Find the red blood cells and label each as P. falciparum-infected, uninfected, or of indeterminate infection status.
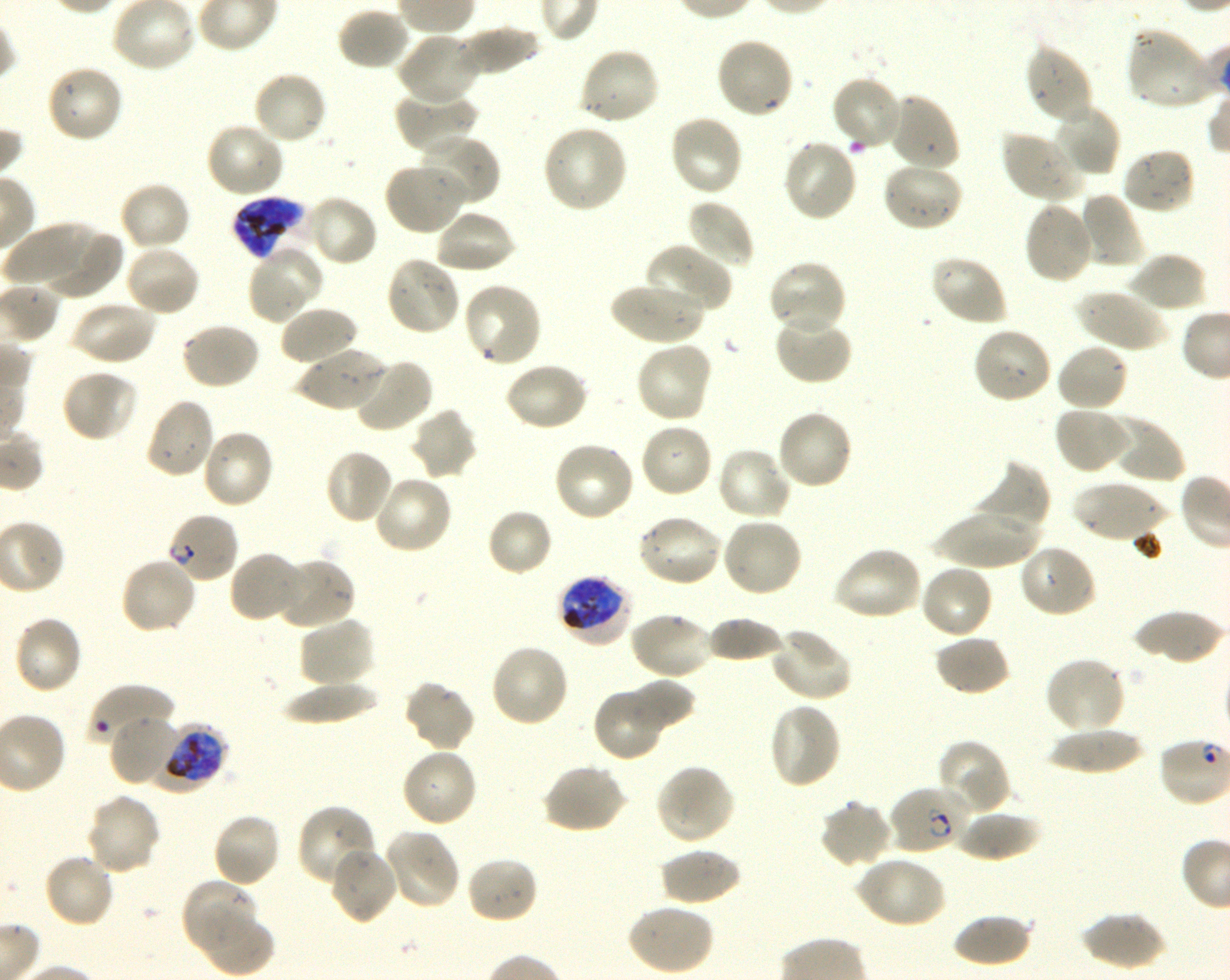
Approximate bounding boxes as {x1, y1, x2, y2} in pixels. Not every red blood cell is marked. A life-cycle stage — or a range of stages, where the recorded stages span more than one — follows each staged infected red blood cell.
Infected red blood cells: {232, 197, 309, 260} late trophozoite to late schizont; {167, 511, 239, 584} ring; {557, 573, 632, 646} early trophozoite to early schizont; {154, 719, 228, 793} late trophozoite to late schizont; {887, 784, 969, 855} ring.
Red blood cells of indeterminate infection status: {88, 684, 173, 749}.
Uninfected red blood cells: {335, 6, 412, 72}, {457, 25, 540, 78}, {1125, 27, 1217, 110}, {396, 33, 480, 106}, {715, 35, 795, 120}, {1025, 43, 1096, 124}, {578, 45, 661, 126}, {45, 63, 124, 144}, {252, 70, 328, 146}, {830, 74, 904, 152}, {394, 90, 479, 157}, {886, 91, 962, 173}, {1051, 102, 1121, 177}, {668, 113, 745, 197}, {206, 121, 286, 199}, {541, 124, 629, 215}, {999, 129, 1087, 205}, {417, 133, 498, 210}, {781, 139, 859, 223}, {1120, 147, 1197, 215}, {383, 161, 467, 236}, {880, 161, 965, 233}, {118, 180, 192, 253}, {1078, 191, 1146, 269}, {303, 194, 379, 267}, {686, 198, 755, 271}, {1022, 200, 1095, 285}, {434, 209, 515, 275}, {4, 222, 97, 290}, {36, 228, 123, 300}, {644, 242, 733, 315}, {123, 243, 201, 317}, {247, 244, 324, 323}, {1125, 251, 1207, 313}, {929, 254, 1007, 327}, {384, 255, 462, 338}, {767, 259, 848, 337}, {462, 281, 544, 368}, {609, 282, 704, 346}, {1075, 286, 1165, 353}, {70, 299, 157, 367}, {278, 304, 359, 368}, {774, 311, 853, 385}, {179, 322, 261, 391}, {972, 326, 1053, 405}, {635, 342, 713, 424}, {1055, 342, 1131, 412}, {296, 347, 386, 412}, {351, 358, 434, 435}, {503, 361, 589, 432}, {60, 368, 138, 443}, {143, 396, 216, 479}, {1053, 406, 1130, 475}, {409, 407, 479, 481}, {776, 409, 855, 491}, {1101, 414, 1186, 483}, {639, 422, 714, 499}, {200, 428, 275, 510}, {552, 441, 636, 523}, {715, 446, 794, 523}, {323, 448, 394, 525}, {973, 460, 1052, 535}, {373, 474, 454, 554}, {1070, 480, 1168, 544}, {932, 506, 1043, 568}, {486, 508, 553, 578}, {636, 513, 723, 588}, {720, 516, 804, 598}, {1018, 544, 1098, 619}, {832, 545, 923, 621}, {228, 550, 304, 623}, {119, 555, 198, 635}, {274, 556, 357, 629}, {918, 563, 994, 642}, {629, 610, 714, 680}, {1131, 610, 1226, 664}, {12, 614, 84, 696}, {704, 616, 787, 663}, {298, 617, 376, 688}, {769, 626, 851, 703}, {933, 634, 1012, 697}, {489, 643, 570, 729}, {1043, 657, 1126, 735}, {625, 678, 695, 732}, {403, 680, 476, 752}, {281, 681, 380, 724}, {592, 688, 667, 762}, {768, 701, 842, 790}, {109, 713, 181, 788}, {1046, 727, 1146, 774}, {937, 739, 1010, 815}, {401, 747, 478, 828}, {542, 763, 628, 834}, {655, 763, 736, 845}, {85, 794, 161, 874}, {818, 800, 893, 869}, {296, 803, 379, 890}, {953, 809, 1042, 861}, {211, 812, 282, 888}, {382, 828, 461, 910}, {327, 846, 397, 926}, {659, 847, 741, 906}, {42, 853, 117, 929}, {465, 855, 539, 925}, {853, 855, 946, 929}, {181, 877, 261, 958}, {625, 902, 714, 976}, {198, 909, 274, 977}, {1080, 911, 1165, 971}, {951, 914, 1034, 967}.

preparation = thin blood smear
field of view = one from this slide
culture = in-vitro P. falciparum strain 3D7, shaking
donor blood group = O+
image size = 1230×980 pixels
objective = 100x, oil immersion, numerical aperture 1.30
stain = Giemsa